Locate every Plasmodium parasite.
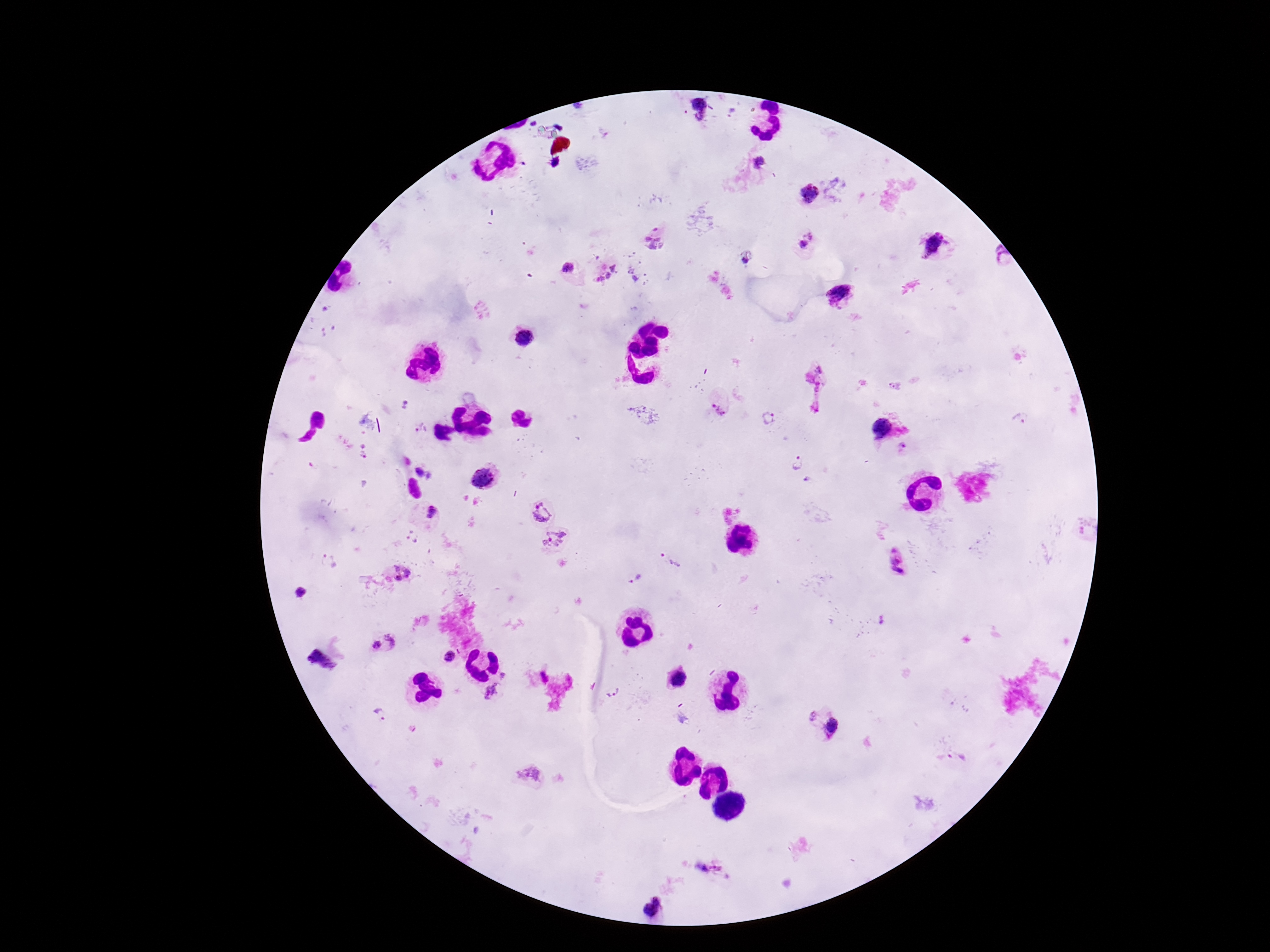
Approximate object centers, in pixels from the top-left corner.
Plasmodium parasites: (x=698, y=106), (x=758, y=163), (x=809, y=194), (x=654, y=239), (x=808, y=241), (x=934, y=245), (x=745, y=260), (x=569, y=268), (x=606, y=271), (x=632, y=274), (x=841, y=294), (x=526, y=337), (x=720, y=405), (x=767, y=418), (x=1021, y=419), (x=420, y=428), (x=883, y=428), (x=905, y=447), (x=796, y=462), (x=484, y=477), (x=541, y=511), (x=431, y=513), (x=556, y=542), (x=896, y=559), (x=670, y=562), (x=398, y=575), (x=634, y=578), (x=300, y=593), (x=383, y=643), (x=449, y=656), (x=321, y=661), (x=506, y=672), (x=677, y=679), (x=492, y=692), (x=613, y=694), (x=828, y=724), (x=529, y=774), (x=651, y=907).

field of view = one from this slide
stain = Giemsa
capture = smartphone camera through the microscope eyepiece
patient malaria status = positive
preparation = thick peripheral-blood smear
magnification = 100x
image size = 1270×952 pixels